Assess the morphology of the erythrocytes.
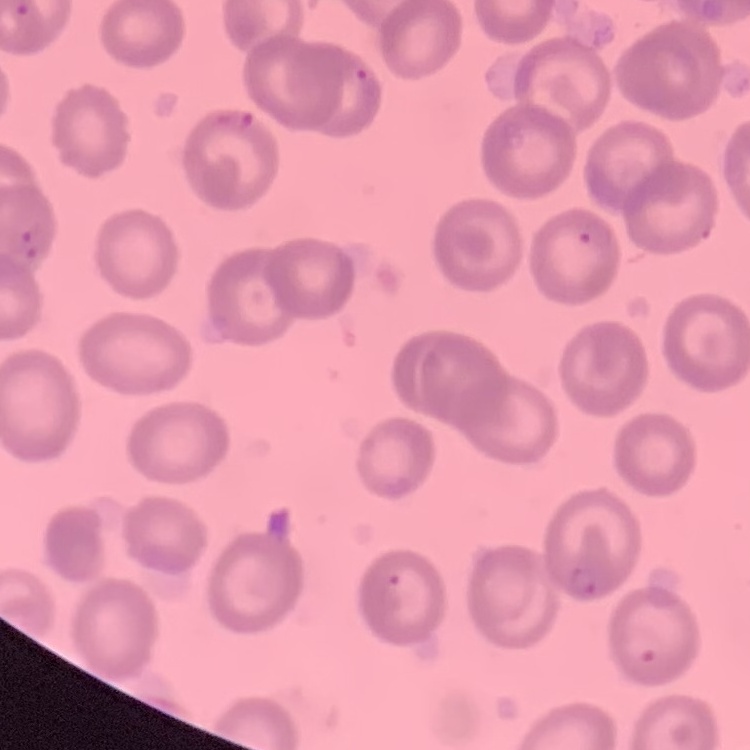

They show no rouleaux formation.

Summary:
  - Preparation: thin blood film
  - Stain: Field's or Giemsa
  - Image type: square crop of a larger photomicrograph